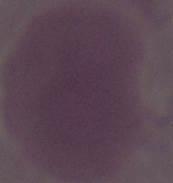

Summary:
  - Identification: erythrocyte
  - Modality: micrograph
  - Magnification: 1000x